Classify this cell by malaria status.
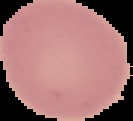
Uninfected.

Summary:
  - Preparation: thin blood film
  - Image type: cell region segmented out of the field of view; surrounding area masked to black
  - Image size: 133×121 pixels